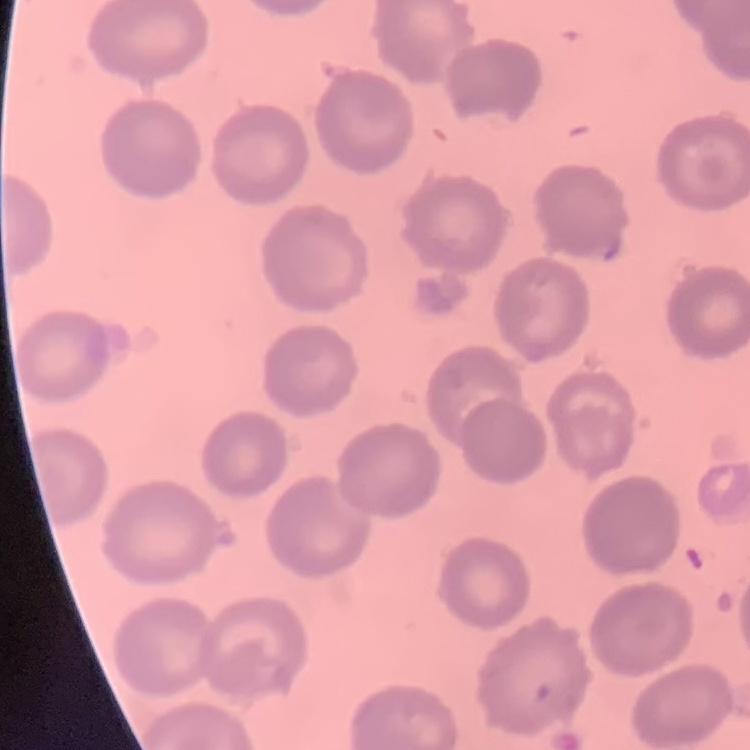
The erythrocytes exhibit no rouleaux formation. Field's or Giemsa stain. Thin blood film. One tile cut from a larger photomicrograph.